Locate every blood parasite and identify its species.
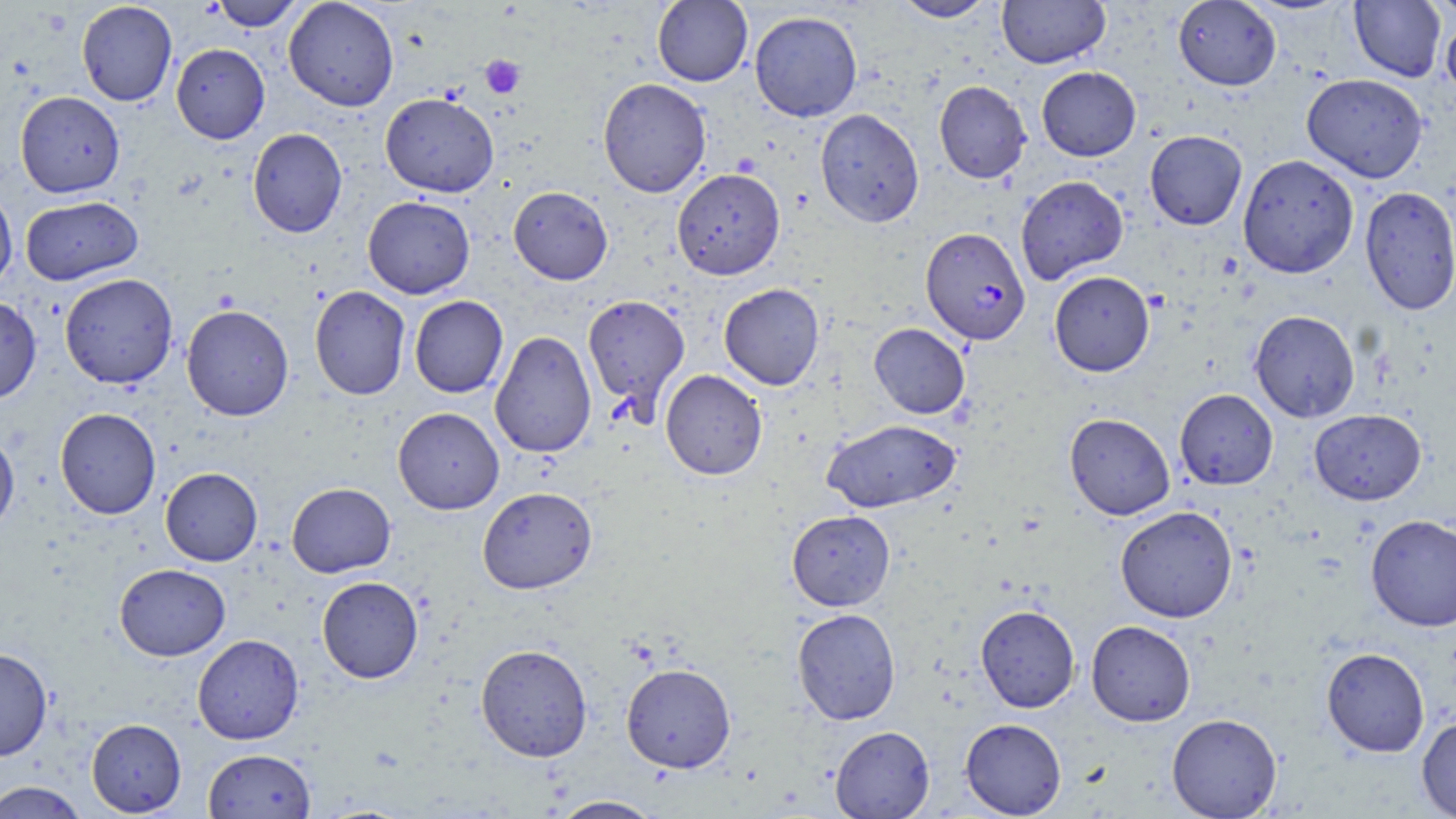
Approximate bounding boxes as [x1, y1, x2, y2] in pixels.
Plasmodium falciparum-infected red blood cells: [920, 227, 1031, 345].
No Plasmodium ovale, Plasmodium malariae, Plasmodium vivax, Babesia divergens, or Trypanosoma brucei observed.

Summary:
  - Uninfected red blood cell locations: [209, 0, 306, 31], [283, 0, 400, 111], [652, 0, 752, 86], [892, 0, 998, 22], [997, 0, 1109, 69], [1349, 0, 1446, 81], [1428, 0, 1456, 22], [1172, 1, 1281, 90], [77, 2, 178, 106], [749, 11, 862, 122], [1441, 14, 1456, 102], [171, 43, 269, 144], [1036, 67, 1141, 161], [1302, 73, 1428, 182], [598, 78, 711, 197], [934, 80, 1031, 183], [15, 91, 125, 197], [380, 92, 499, 196], [815, 108, 924, 227], [247, 128, 347, 237], [1145, 130, 1247, 230], [1238, 154, 1359, 278], [672, 168, 785, 280], [1015, 175, 1128, 285], [0, 185, 18, 291], [508, 186, 613, 284], [1360, 186, 1456, 316], [19, 196, 143, 285], [363, 196, 475, 298], [1049, 271, 1155, 376], [59, 273, 178, 388], [719, 283, 825, 390], [309, 285, 410, 400], [582, 293, 690, 416], [409, 295, 508, 398], [0, 296, 41, 404], [181, 305, 294, 421], [1249, 310, 1360, 422], [869, 323, 970, 419], [490, 330, 596, 458], [660, 369, 767, 480], [1175, 388, 1278, 490], [393, 407, 504, 514], [55, 408, 161, 519], [1309, 409, 1426, 505], [1064, 412, 1176, 520], [821, 418, 961, 512], [0, 428, 19, 535], [160, 467, 263, 566], [287, 482, 396, 577], [478, 486, 597, 594], [1115, 506, 1238, 623], [786, 510, 896, 610], [1365, 514, 1456, 631], [115, 563, 231, 661], [316, 576, 424, 683], [975, 604, 1080, 712], [791, 608, 901, 724], [1086, 620, 1196, 726], [193, 634, 304, 744], [475, 643, 593, 761], [0, 647, 53, 761], [1321, 647, 1429, 757], [621, 663, 736, 773], [1166, 713, 1282, 818], [1417, 715, 1456, 818], [86, 718, 186, 816], [960, 718, 1067, 817], [829, 725, 935, 818], [203, 748, 316, 819], [0, 781, 89, 819], [548, 795, 664, 818]
  - Platelet locations: [480, 55, 525, 99]
  - Slide-level diagnosis: Plasmodium falciparum
  - Preparation: thin blood film
  - Stain: May-Grünwald-Giemsa
  - Image size: 1456×819 pixels
  - Field of view: single
  - Modality: light microscopy
  - Magnification: 1000x